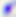 Photomicrograph. 400x magnification. Toxoplasma gondii is shown.